Report the malaria status of this cell.
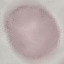
Uninfected.

image type = automatically extracted cell patch, resized to 64 × 64 pixels
stain = Giemsa
preparation = thin blood film
capture = smartphone camera at the microscope eyepiece